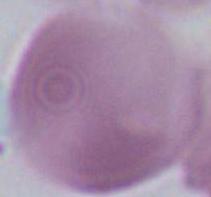

identification = red blood cell
modality = micrograph
magnification = 1000x